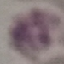

{
  "result": "no malaria parasites detected",
  "capture": "smartphone camera at the microscope eyepiece",
  "preparation": "thin smear",
  "stain": "Giemsa",
  "image_type": "cell patch, automatically extracted from a larger field of view and resized to 64 × 64 pixels"
}